Assess this cell for malaria.
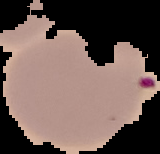

Parasitized.

Summary:
  - Image type: segmented cell region with the area outside set to black
  - Image size: 160×154 pixels
  - Preparation: thin blood smear